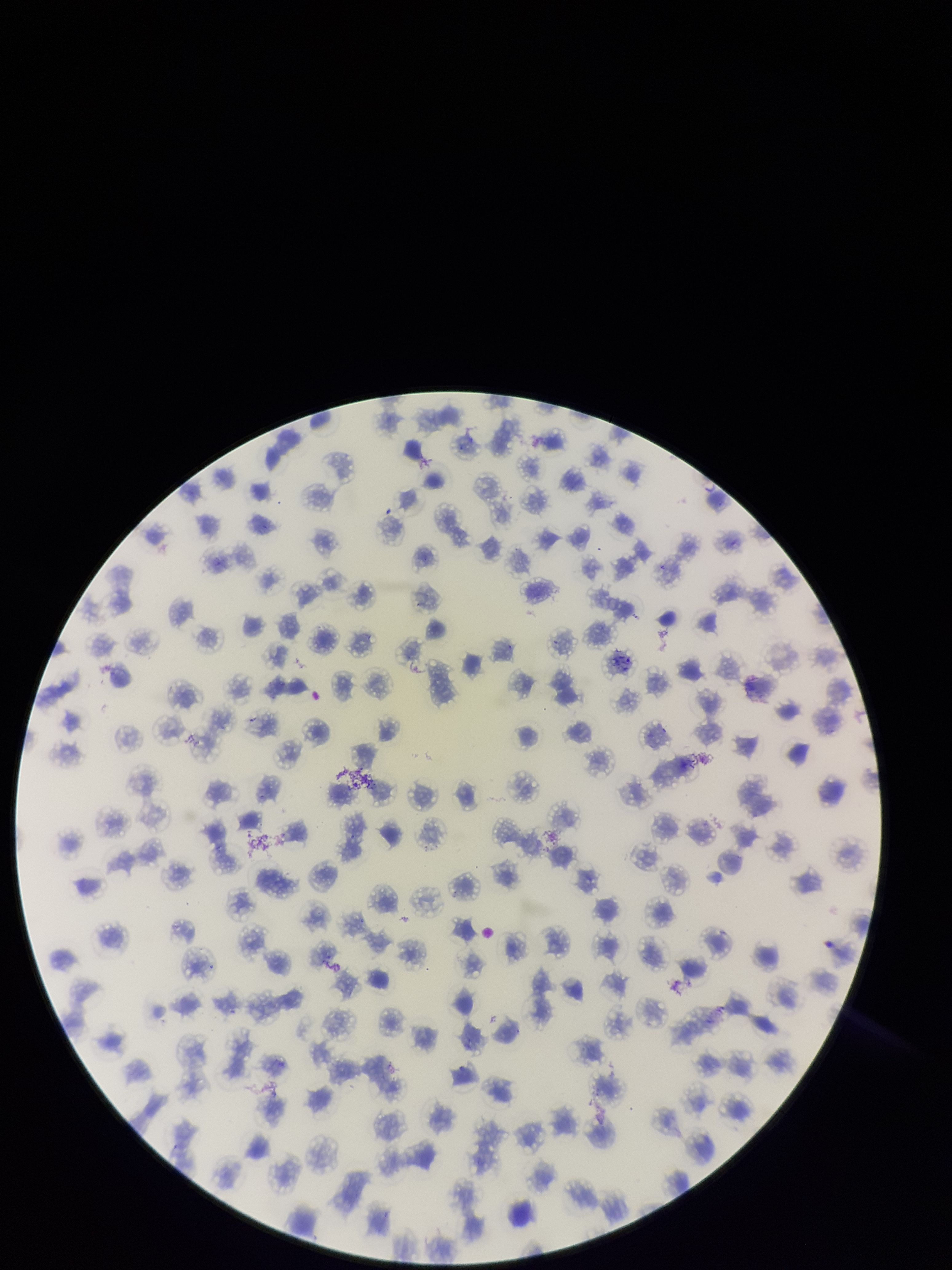

Patient malaria status: infected. Smartphone photograph taken through the eyepiece of a microscope. Image is 952×1270 pixels. Parasitized red blood cells: none detected. Red blood cell count: 179. Preparation: thin. Parasitized red blood cell count: 0. Giemsa stain. Single field of view. Species reported for this patient: Plasmodium falciparum.